Classify this cell by malaria status.
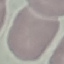

It is uninfected.

Summary:
  - Preparation: thin blood smear
  - Capture: smartphone through the microscope eyepiece
  - Stain: Giemsa
  - Image type: cell patch, automatically extracted from a larger field of view and resized to 64 × 64 pixels